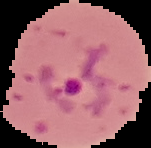

Summary:
  - Image type: segmented cell region with the area outside set to black
  - Malaria status: parasitized
  - Preparation: thin blood film
  - Image size: 151×148 pixels